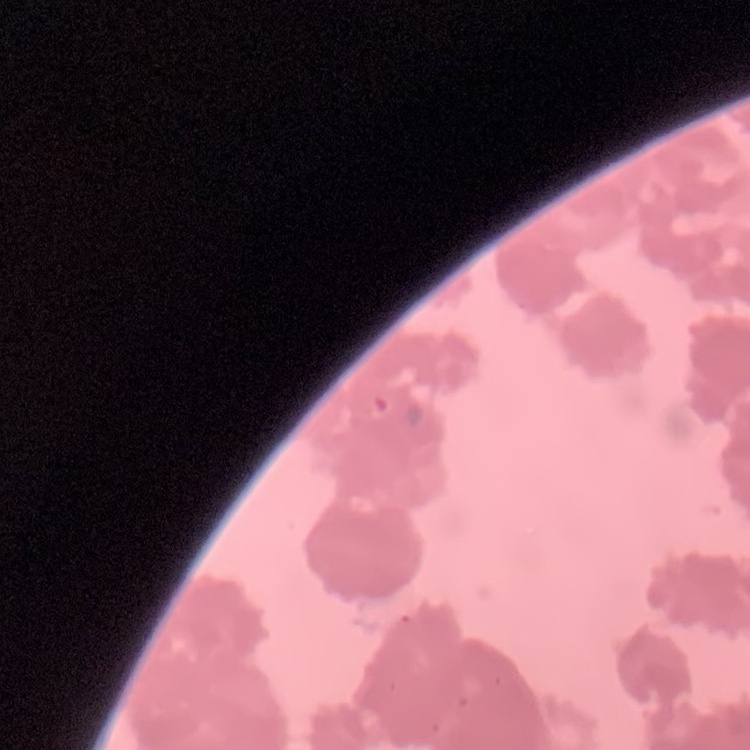
The erythrocytes exhibit rouleaux formation. Thin peripheral smear. Field's or Giemsa stain. One tile cut from a larger photomicrograph.